State which parasite is depicted.
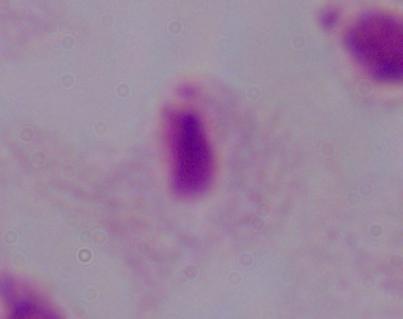
This is a trichomonad.

Summary:
  - Modality: micrograph
  - Magnification: 1000x